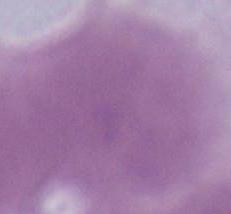
Summary:
  - Magnification: 1000x
  - Identification: erythrocyte
  - Modality: micrograph